Give the position of every Plasmodium parasite.
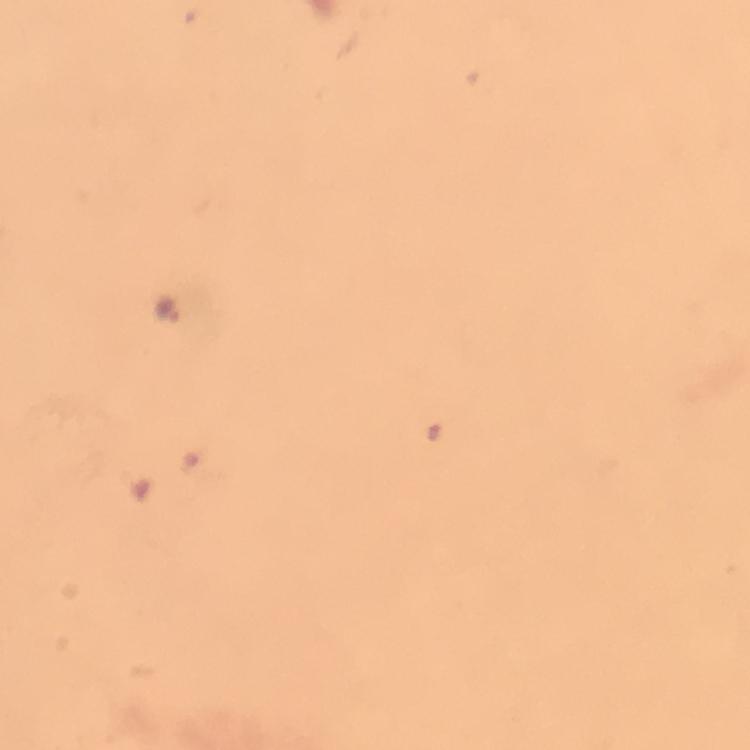
Approximate centers as (x, y) in pixels.
Plasmodium parasites: (165, 309).

From a malaria diagnostic workup. Smartphone photograph taken through a microscope. Giemsa-stained preparation. Image is 750×750 pixels. Thick smear. 100x magnification. Cropped region of a single field of view. Immersion oil applied.